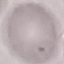

Result: negative for malaria parasites. Thin blood film. Acquired by smartphone through the microscope eyepiece. Giemsa-stained preparation. Automatically extracted cell patch, resized to 64 × 64 pixels.